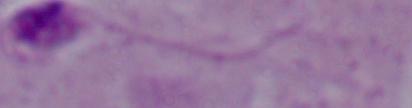
Captured at 1000x magnification. Photomicrograph. A Leishmania parasite is seen.